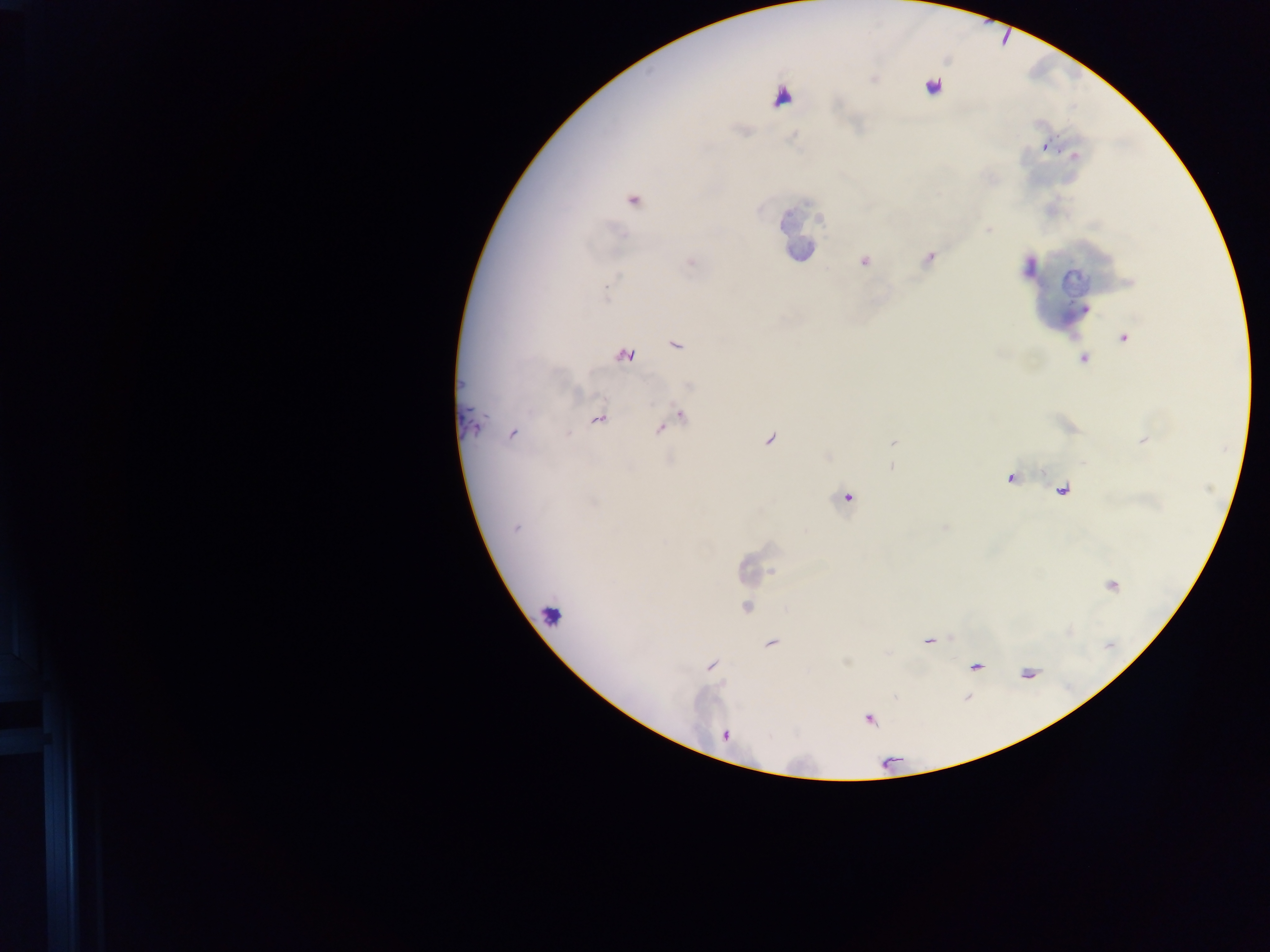
Approximate centers as x y in pixels. Leukocyte locations: 554 615. Malaria parasite locations: 932 87; 1045 147; 633 200; 930 257; 864 261; 691 262; 606 292; 1124 337; 675 344; 624 356; 1083 359; 680 416; 598 420; 472 425; 512 434; 770 439; 847 498; 516 529; 746 607; 771 643; 711 665; 869 720. Collected in Ghana. Mobile-phone photograph taken through the microscope. Thick blood smear. Image is 1270×952 pixels. One field of view.